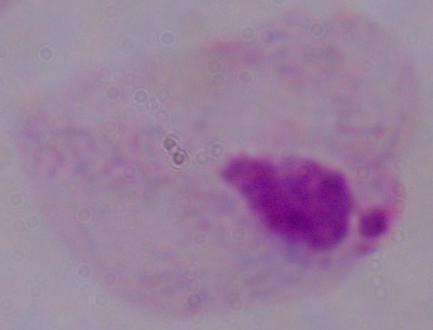

identification = trichomonad
modality = photomicrograph
magnification = 1000x